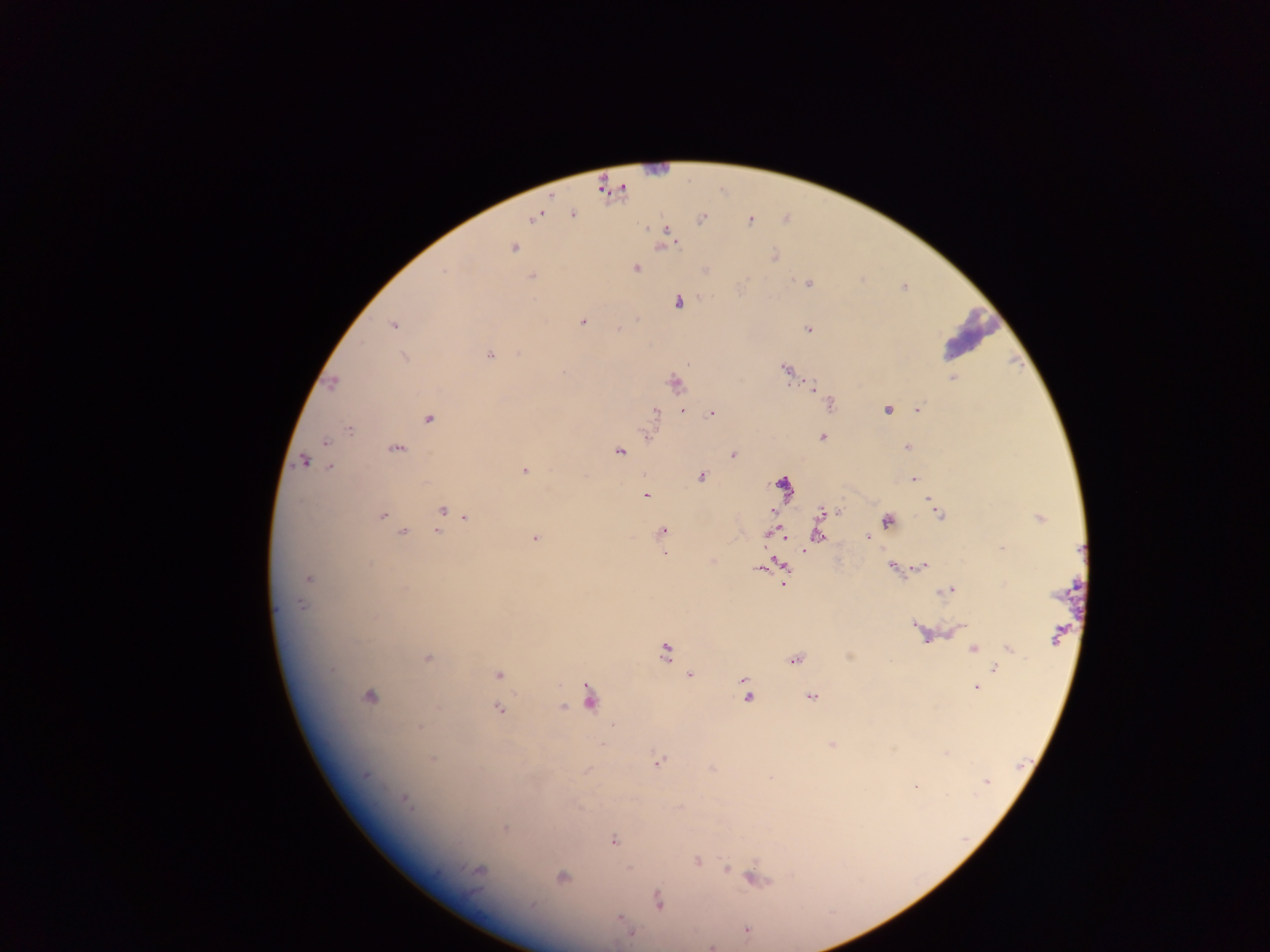

Approximate centers as {x, y} in pixels. Plasmodium parasite locations: {572, 215}, {534, 217}, {702, 219}, {751, 222}, {668, 232}, {512, 248}, {774, 256}, {635, 268}, {444, 271}, {531, 277}, {807, 284}, {678, 302}, {583, 322}, {393, 325}, {619, 328}, {808, 329}, {489, 355}, {404, 357}, {785, 368}, {563, 373}, {952, 378}, {332, 384}, {675, 384}, {811, 386}, {830, 404}, {919, 408}, {683, 410}, {887, 410}, {655, 413}, {713, 414}, {429, 419}, {349, 430}, {646, 433}, {822, 437}, {326, 442}, {907, 447}, {396, 448}, {619, 452}, {733, 455}, {303, 462}, {330, 467}, {524, 470}, {701, 477}, {914, 479}, {782, 484}, {645, 496}, {442, 510}, {773, 512}, {824, 512}, {838, 512}, {938, 514}, {382, 516}, {465, 517}, {1040, 518}, {887, 520}, {663, 531}, {402, 532}, {438, 532}, {775, 534}, {817, 534}, {782, 536}, {868, 538}, {535, 539}, {1001, 548}, {804, 551}, {664, 554}, {923, 565}, {784, 567}, {892, 567}, {758, 569}, {308, 578}, {784, 583}, {406, 588}, {949, 589}, {301, 604}, {374, 618}, {916, 625}, {960, 627}, {925, 636}, {1055, 637}, {973, 649}, {1009, 649}, {665, 652}, {427, 658}, {795, 659}, {995, 668}, {333, 670}, {498, 674}, {689, 675}, {744, 680}, {976, 688}, {368, 697}, {747, 697}, {811, 697}, {590, 698}, {563, 707}, {499, 708}, {419, 728}, {603, 744}, {831, 745}, {946, 753}, {432, 760}, {658, 762}, {588, 770}, {366, 775}, {987, 781}, {916, 786}, {406, 801}, {505, 828}, {614, 841}, {697, 861}, {727, 868}, {478, 871}, {562, 878}, {756, 879}, {659, 901}, {532, 905}, {621, 920}, {746, 929}, {631, 933}, {711, 947}. Thick blood smear. Collected in Ghana. Image is 1270×952 pixels. Single field of view. Mobile-phone photograph taken through the microscope.